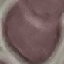
Summary:
  - Malaria status: uninfected
  - Stain: Giemsa
  - Preparation: thin smear
  - Capture: smartphone through the microscope eyepiece
  - Image type: cell patch, automatically extracted from a larger field of view and resized to 64 × 64 pixels